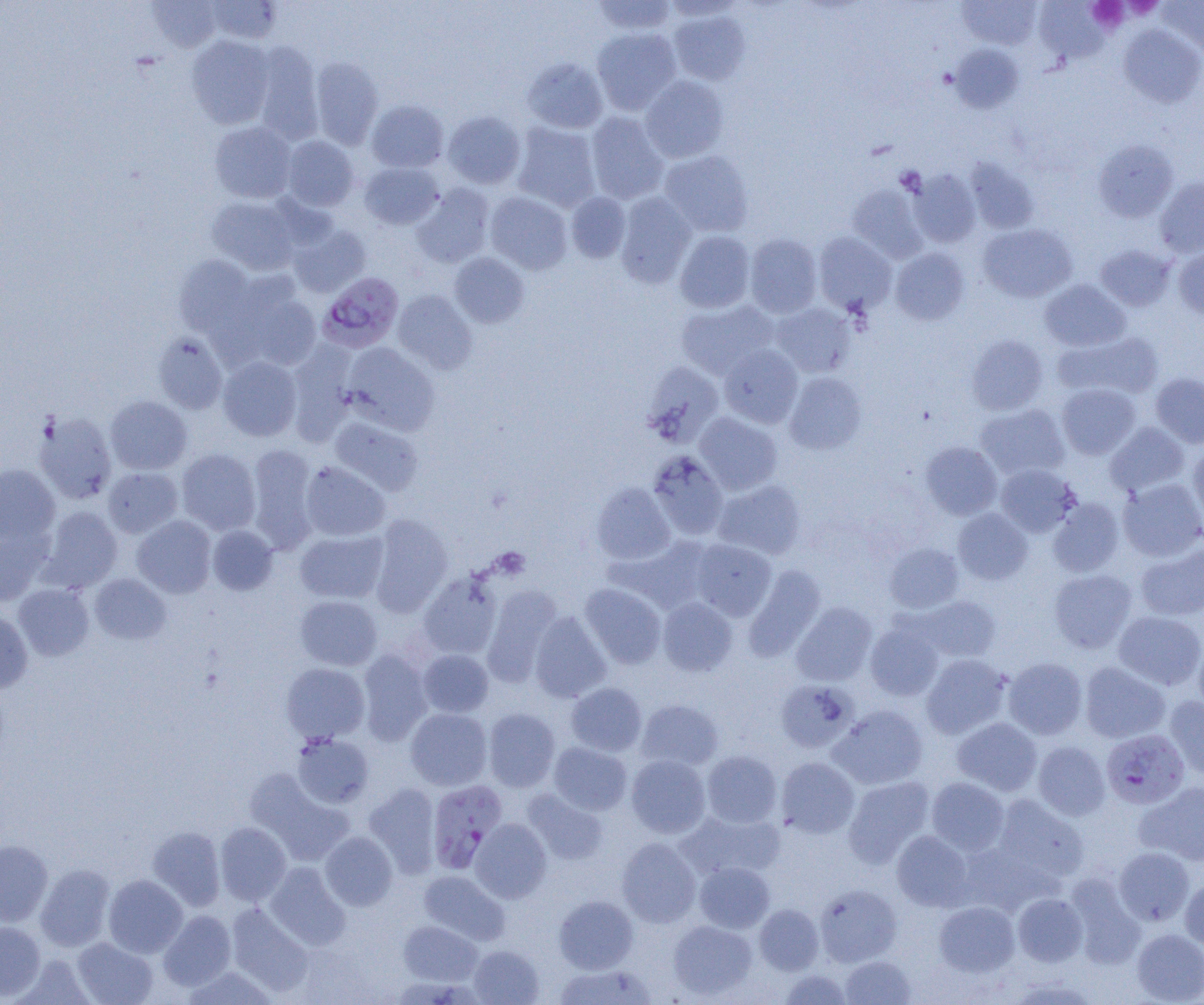

Summary:
  - Coordinate format: approximate bounding boxes as (x1,y1)-(x2,y2) corner pairs in pixels
  - Uninfected red blood cell locations: (147,0)-(221,52), (206,0)-(283,44), (662,0)-(746,20), (958,0)-(1041,49), (1158,0)-(1204,54), (592,1)-(677,35), (1034,2)-(1109,64), (668,9)-(750,85), (1119,25)-(1204,107), (592,27)-(681,114), (187,35)-(274,127), (252,43)-(323,143), (950,45)-(1025,114), (310,57)-(383,149), (522,57)-(608,133), (640,75)-(728,163), (366,100)-(449,172), (443,111)-(525,188), (586,112)-(669,204), (209,121)-(297,203), (512,122)-(601,211), (282,135)-(359,211), (1093,139)-(1179,223), (659,150)-(754,237), (965,157)-(1041,235), (360,162)-(443,230), (906,168)-(981,248), (1155,178)-(1204,258), (412,184)-(494,268), (847,184)-(928,263), (485,192)-(572,274), (566,192)-(631,263), (615,192)-(696,288), (207,195)-(302,275), (288,223)-(370,297), (978,224)-(1077,302), (675,230)-(755,313), (813,232)-(896,316), (745,234)-(822,317), (1095,244)-(1175,311), (890,247)-(969,325), (1174,247)-(1204,319), (449,253)-(530,328), (174,255)-(258,340), (227,278)-(321,371), (1040,279)-(1130,351), (393,290)-(477,374), (676,300)-(779,379), (771,303)-(856,377), (1053,331)-(1163,402), (153,332)-(228,414), (967,334)-(1048,415), (286,343)-(358,444), (342,343)-(440,435), (718,344)-(803,428), (218,356)-(302,441), (642,362)-(724,447), (784,373)-(867,454), (1151,373)-(1204,448), (1057,383)-(1141,459), (106,396)-(192,474), (975,404)-(1070,479), (34,412)-(117,504), (695,412)-(782,495), (330,417)-(424,496), (1105,422)-(1189,497), (921,442)-(1002,519), (246,444)-(319,551), (1189,445)-(1204,528), (176,449)-(261,535), (648,451)-(728,540), (301,461)-(390,541), (0,464)-(60,545), (995,464)-(1080,537), (103,467)-(183,538), (1118,478)-(1204,561), (713,480)-(806,560), (591,482)-(675,565), (1048,498)-(1124,576), (39,506)-(123,592), (953,508)-(1032,585), (370,514)-(453,615), (132,516)-(216,597), (208,525)-(278,595), (0,526)-(51,606), (295,530)-(388,603), (612,536)-(715,613), (690,539)-(776,621), (884,543)-(964,613), (1136,543)-(1204,621), (744,565)-(826,662), (1049,569)-(1136,653), (90,573)-(171,644), (418,573)-(500,659), (14,583)-(94,660), (580,583)-(666,668), (482,586)-(562,685), (295,595)-(382,670), (917,596)-(1001,662), (658,598)-(738,676), (791,602)-(877,686), (0,611)-(33,692), (1113,611)-(1204,690), (529,612)-(611,702), (865,621)-(944,701), (1193,638)-(1204,718), (418,649)-(494,717), (357,650)-(433,745), (922,654)-(1010,738), (1003,657)-(1087,739), (281,662)-(370,745), (1080,662)-(1170,743), (776,679)-(859,753), (566,682)-(647,755), (1164,696)-(1204,779), (636,699)-(723,772), (829,705)-(928,790), (483,707)-(560,792), (405,708)-(492,790), (952,717)-(1042,796), (291,733)-(375,808), (1032,741)-(1110,820), (549,742)-(632,815), (702,750)-(782,827), (626,754)-(711,838), (776,757)-(860,838), (245,769)-(354,865), (844,776)-(934,866), (926,777)-(1009,855), (1136,781)-(1204,866), (364,783)-(441,876), (523,789)-(609,865), (992,795)-(1088,883), (678,810)-(784,882), (470,818)-(552,903), (215,822)-(292,906), (147,826)-(226,911), (320,831)-(398,910), (892,831)-(973,911), (617,837)-(701,927), (0,841)-(52,926), (1114,847)-(1194,926), (694,862)-(775,933), (264,863)-(350,949), (36,864)-(114,951), (418,870)-(510,944), (1066,873)-(1145,968), (104,874)-(187,957), (1180,875)-(1204,950), (815,884)-(901,966), (1013,893)-(1088,966), (554,895)-(638,973), (934,901)-(1020,976), (226,903)-(313,995), (754,903)-(823,975), (158,910)-(236,990), (398,920)-(482,986), (668,920)-(757,999), (0,922)-(45,1000), (1132,928)-(1204,1004), (72,937)-(158,1005), (469,945)-(544,1004), (16,955)-(96,1004), (840,955)-(917,1004), (552,963)-(658,1004), (182,966)-(278,1004), (779,969)-(852,1005)
  - Plasmodium falciparum-infected red blood cell locations: (318,272)-(404,353), (1101,729)-(1189,810), (427,780)-(507,873)
  - Platelet locations: (1088,0)-(1128,30)
  - Slide-level diagnosis: Plasmodium falciparum
  - Magnification: 1000x
  - Field of view: single
  - Modality: light microscopy
  - Image size: 1204×1005 pixels
  - Preparation: thin blood film